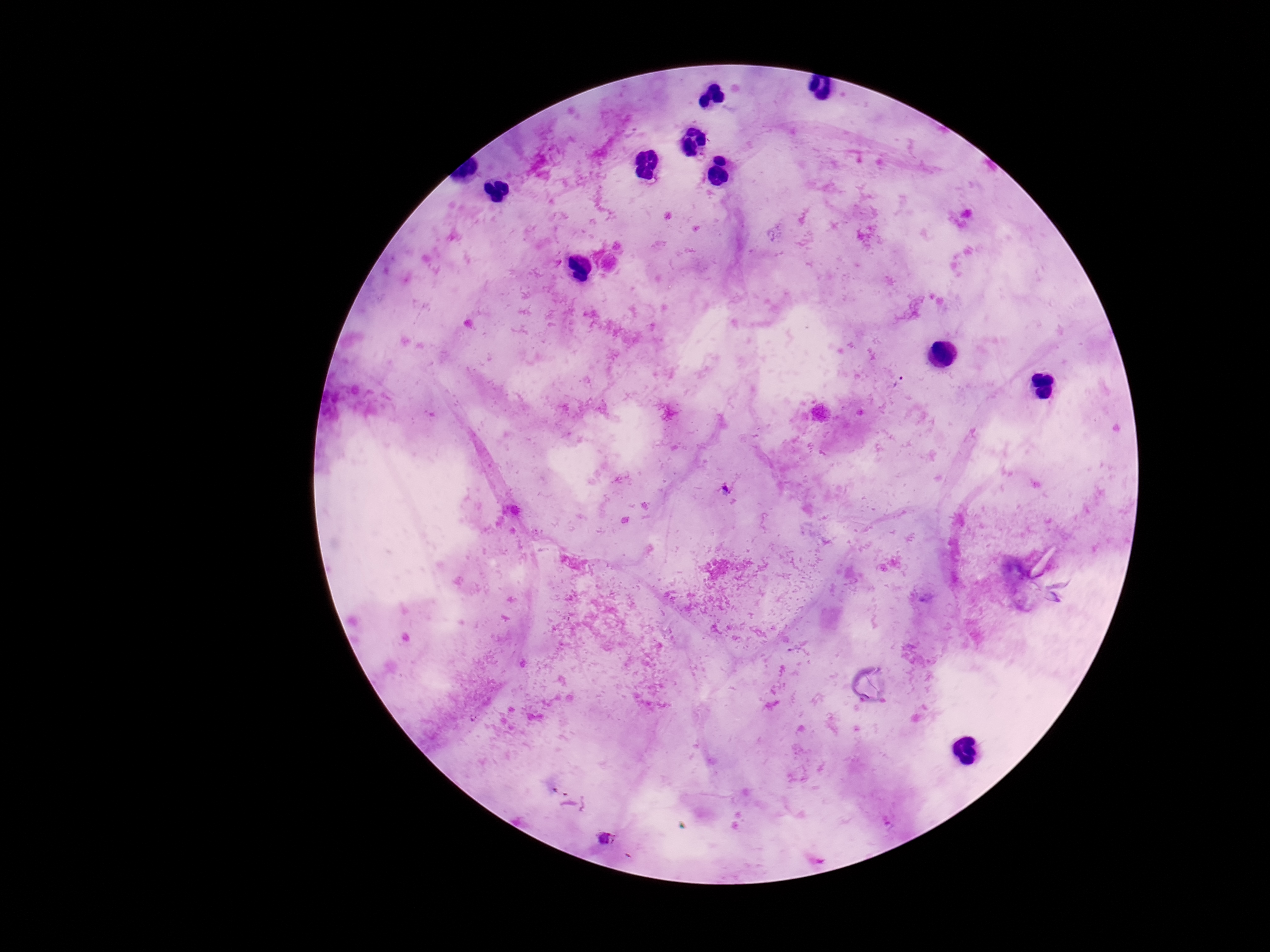
Approximate object centers, in pixels from the top-left corner.
Summary:
  - Plasmodium parasite locations: (x=901, y=382), (x=726, y=491), (x=606, y=840)
  - Patient malaria status: positive
  - Magnification: 100x
  - Preparation: thick peripheral-blood smear
  - Field of view: single
  - Image size: 1270×952 pixels
  - Capture: smartphone camera through the microscope eyepiece
  - Stain: Giemsa